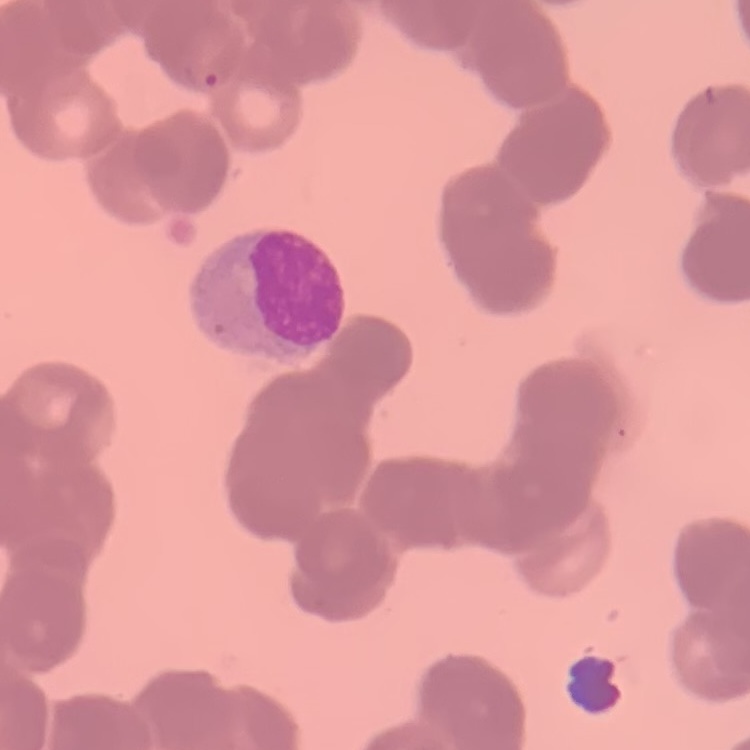
Summary:
  - Red blood cell morphology: rouleaux formation
  - Preparation: thin blood film
  - Stain: Field's or Giemsa
  - Image type: square crop of a larger photomicrograph